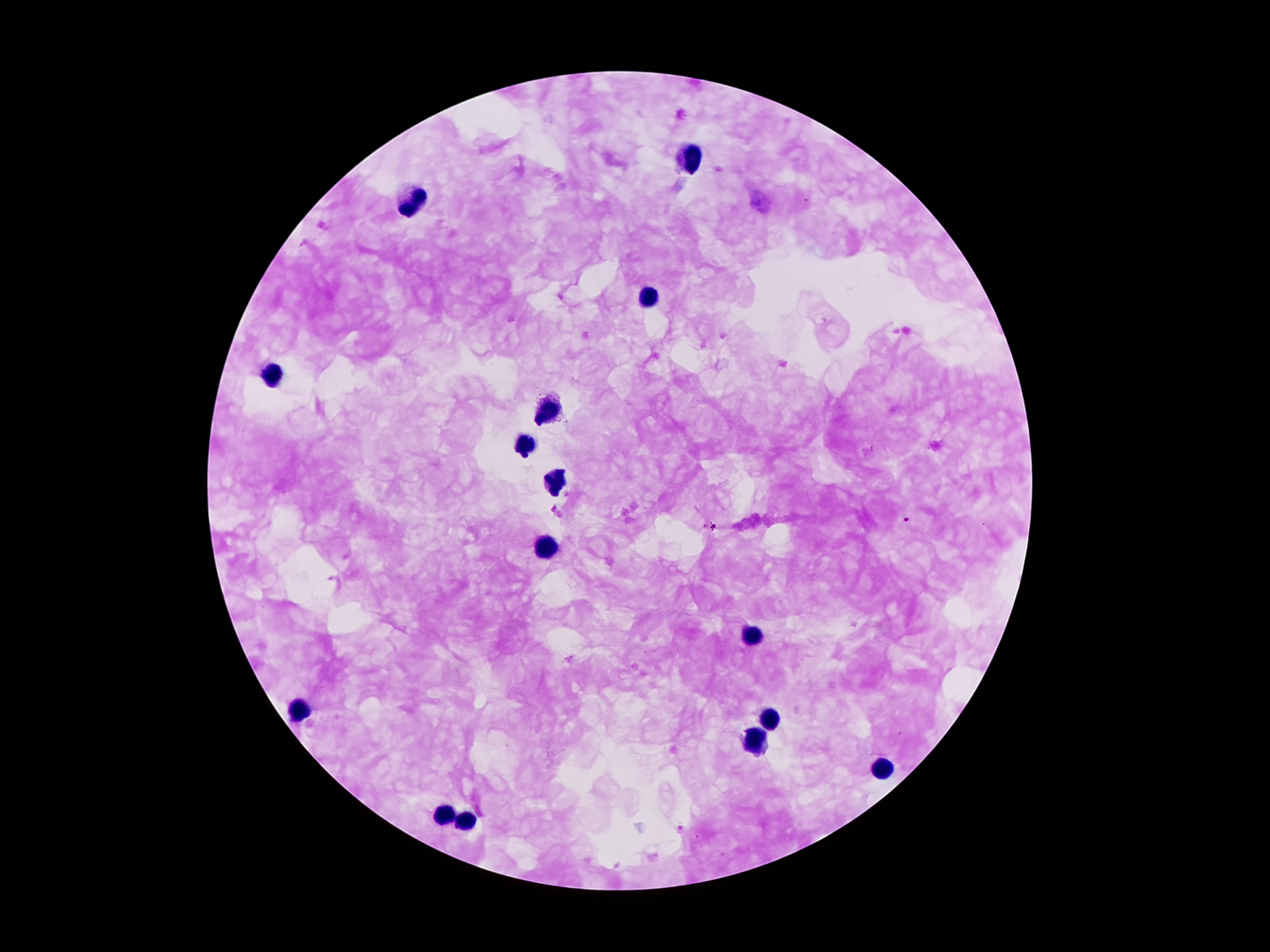

Approximate centers as [x, y] in pixels. Leukocyte locations: [690, 158], [413, 201], [645, 298], [273, 376], [548, 412], [525, 448], [555, 482], [546, 550], [750, 635], [299, 712], [772, 719], [754, 741], [881, 770], [444, 814], [461, 823]. Plasmodium parasite locations: [906, 520], [711, 526]. Patient malaria status: infected with Plasmodium falciparum. Smartphone photograph taken through the microscope eyepiece. 100x magnification. Giemsa stain. Image is 1270×952 pixels. Thick blood smear. One field from this slide.